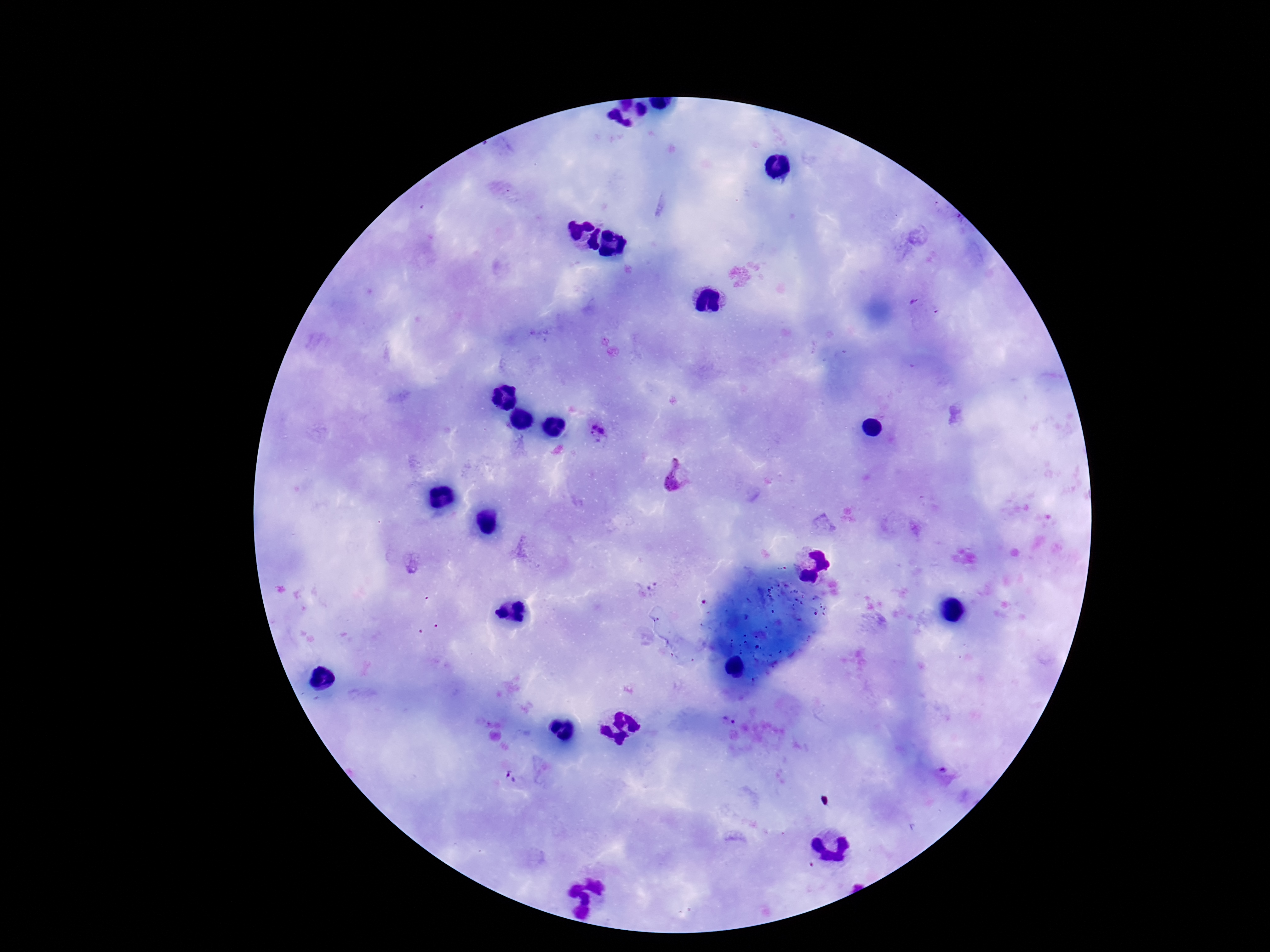
Approximate centers as (x, y) in pixels.
Summary:
  - Plasmodium parasite locations: (599, 431), (676, 476), (727, 722), (510, 776)
  - Stain: Giemsa
  - Preparation: thick blood smear
  - Patient malaria status: positive
  - Capture: smartphone camera through the microscope eyepiece
  - Field of view: single
  - Image size: 1270×952 pixels
  - Magnification: 100x